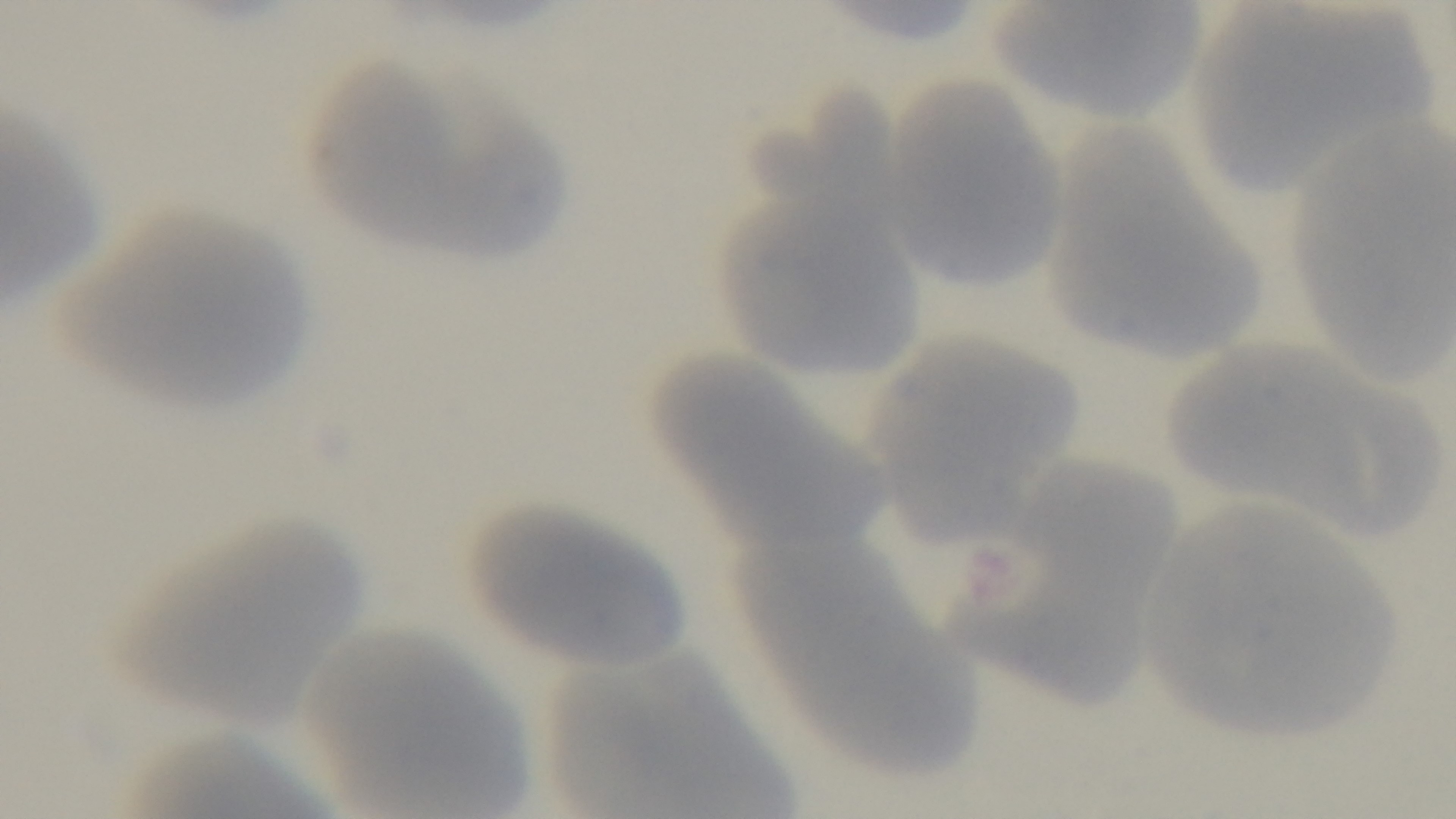
Summary:
  - Objective: 100x oil immersion
  - Capture: mounted 4K digital camera
  - Preparation: thin
  - Stain: Giemsa
  - Field of view: single
  - Modality: light microscopy
  - Malaria status: negative